Give the extent of all uninfected red blood cells.
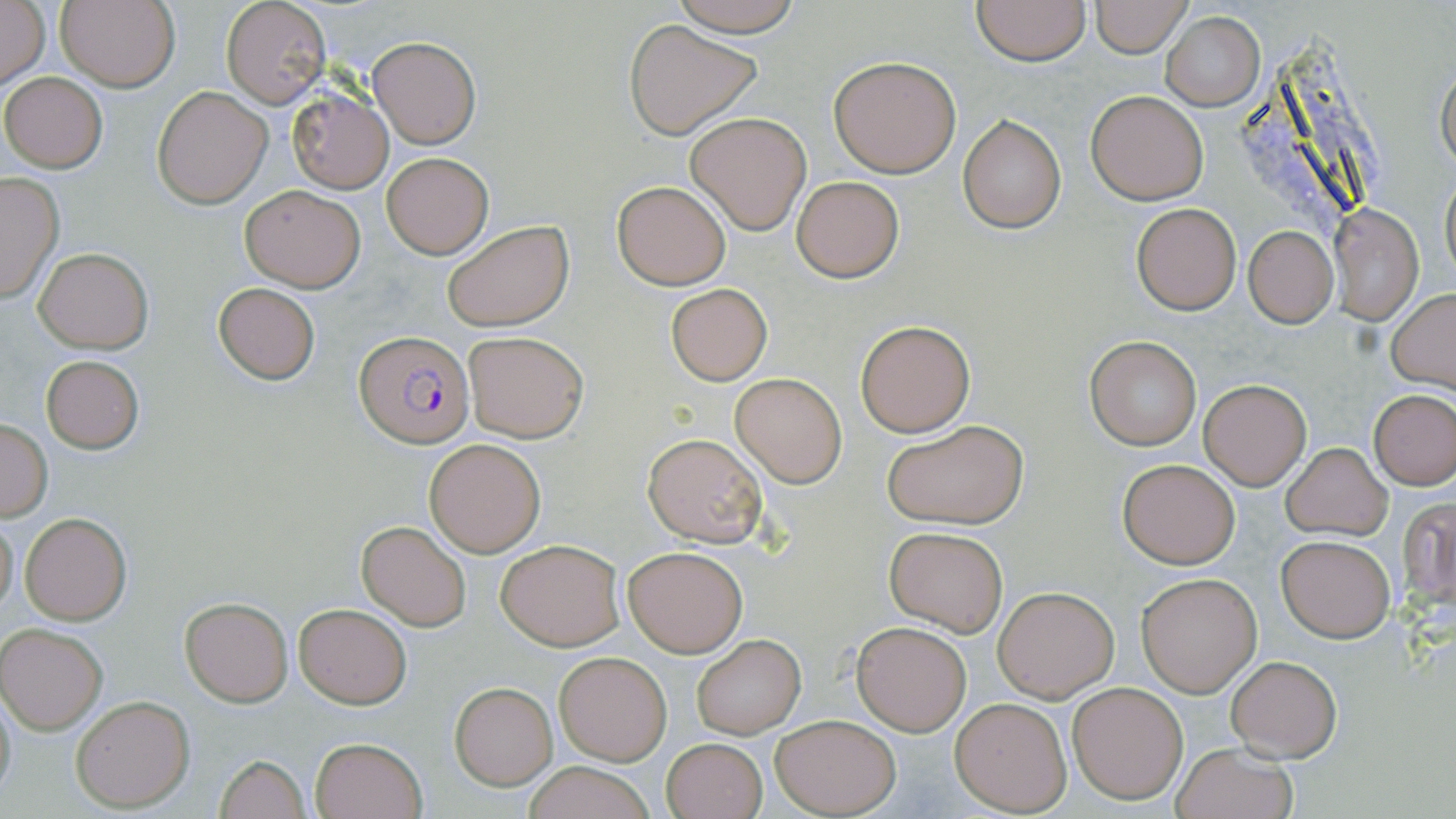
Approximate bounding boxes as [x1, y1, x2, y2] in pixels.
Uninfected red blood cells: [57, 0, 180, 92], [666, 0, 807, 38], [1089, 0, 1191, 55], [1, 1, 50, 92], [221, 1, 329, 108], [970, 1, 1091, 66], [1162, 11, 1264, 110], [624, 20, 760, 139], [368, 35, 481, 149], [828, 56, 962, 177], [1437, 60, 1456, 175], [1, 71, 107, 171], [152, 85, 273, 208], [286, 90, 393, 192], [1086, 90, 1209, 205], [685, 112, 811, 233], [957, 113, 1067, 234], [381, 152, 494, 258], [1440, 164, 1455, 289], [0, 174, 64, 303], [791, 175, 904, 282], [612, 180, 730, 289], [239, 183, 365, 292], [1132, 203, 1241, 315], [1329, 204, 1424, 325], [440, 218, 574, 332], [1245, 226, 1337, 326], [33, 247, 153, 352], [211, 283, 321, 385], [664, 284, 773, 385], [1386, 290, 1456, 391], [854, 319, 975, 437], [462, 329, 590, 443], [1085, 335, 1200, 448], [40, 355, 144, 454], [729, 374, 848, 488], [1198, 378, 1311, 490], [1370, 388, 1455, 491], [881, 419, 1030, 529], [1, 420, 52, 521], [641, 431, 769, 547], [425, 440, 545, 556], [1282, 442, 1392, 540], [1117, 458, 1239, 568], [1397, 496, 1455, 608], [20, 512, 132, 625], [1, 513, 19, 618], [357, 520, 471, 630], [884, 526, 1009, 636], [1276, 535, 1395, 642], [495, 538, 623, 650], [623, 544, 749, 658], [1136, 571, 1262, 697], [993, 586, 1118, 702], [182, 598, 294, 705], [293, 602, 412, 708], [851, 621, 971, 736], [1, 624, 107, 733], [692, 634, 805, 738], [554, 648, 673, 764], [1225, 653, 1343, 762], [1067, 681, 1189, 803], [449, 683, 557, 789], [0, 684, 18, 808], [71, 695, 195, 812], [949, 697, 1072, 816], [770, 713, 901, 817], [308, 735, 428, 819], [661, 737, 767, 819], [1170, 742, 1297, 819], [212, 754, 311, 819], [519, 761, 661, 819].

slide-level diagnosis = Plasmodium falciparum
modality = optical microscopy
magnification = 1000x
image size = 1456×819 pixels
Plasmodium falciparum-infected red blood cell locations = approximate bounding boxes as [x1, y1, x2, y2] in pixels: [356, 331, 475, 447]
field of view = single
preparation = thin blood smear
stain = May-Grünwald-Giemsa